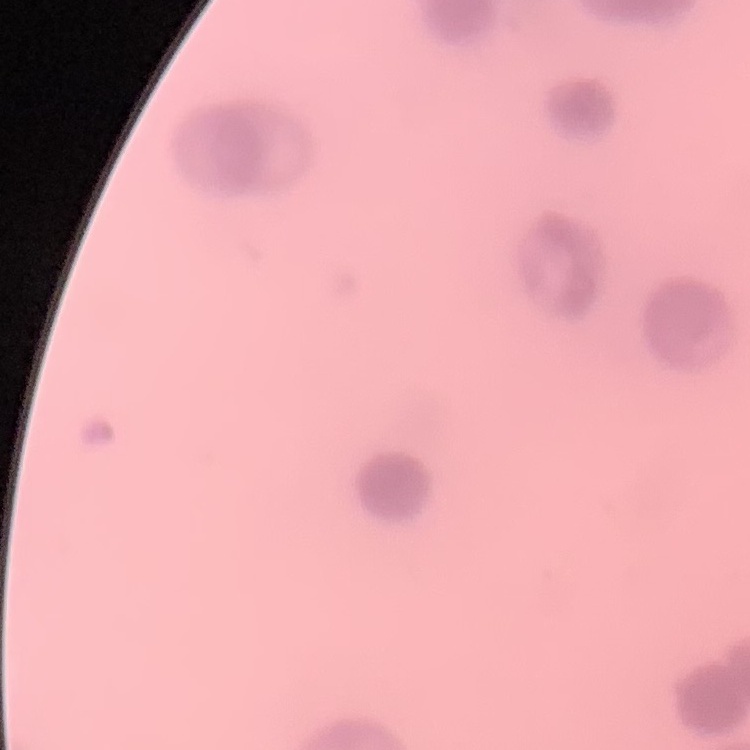
{
  "red_blood_cell_morphology": "rouleaux formation",
  "preparation": "thin blood smear",
  "stain": "Field's or Giemsa",
  "image_type": "square crop of a larger photomicrograph"
}